Describe the morphology of the red blood cells.
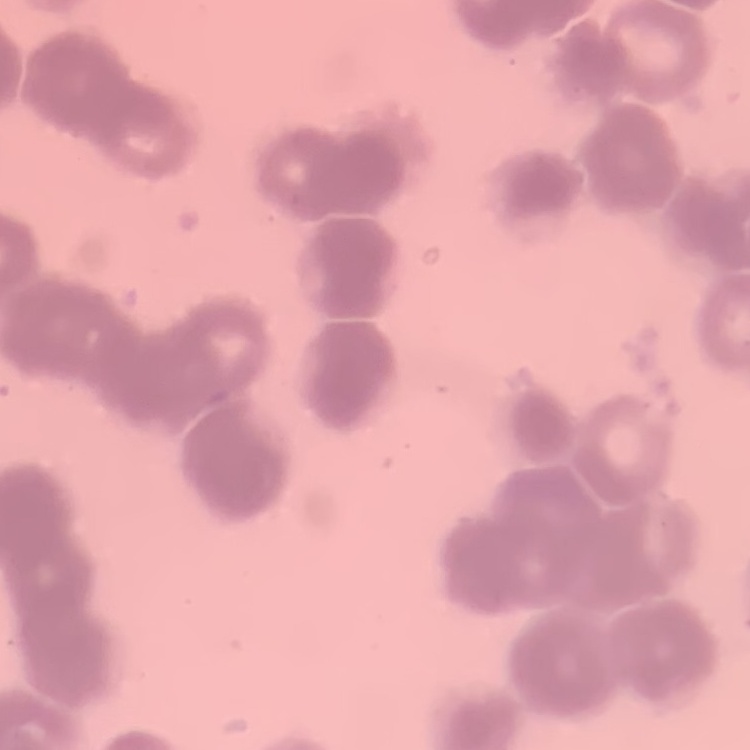

They show rouleaux formation.

image type = one tile cut from a larger photomicrograph
preparation = thin blood film
stain = Field's or Giemsa